Outline each uninfected red blood cell.
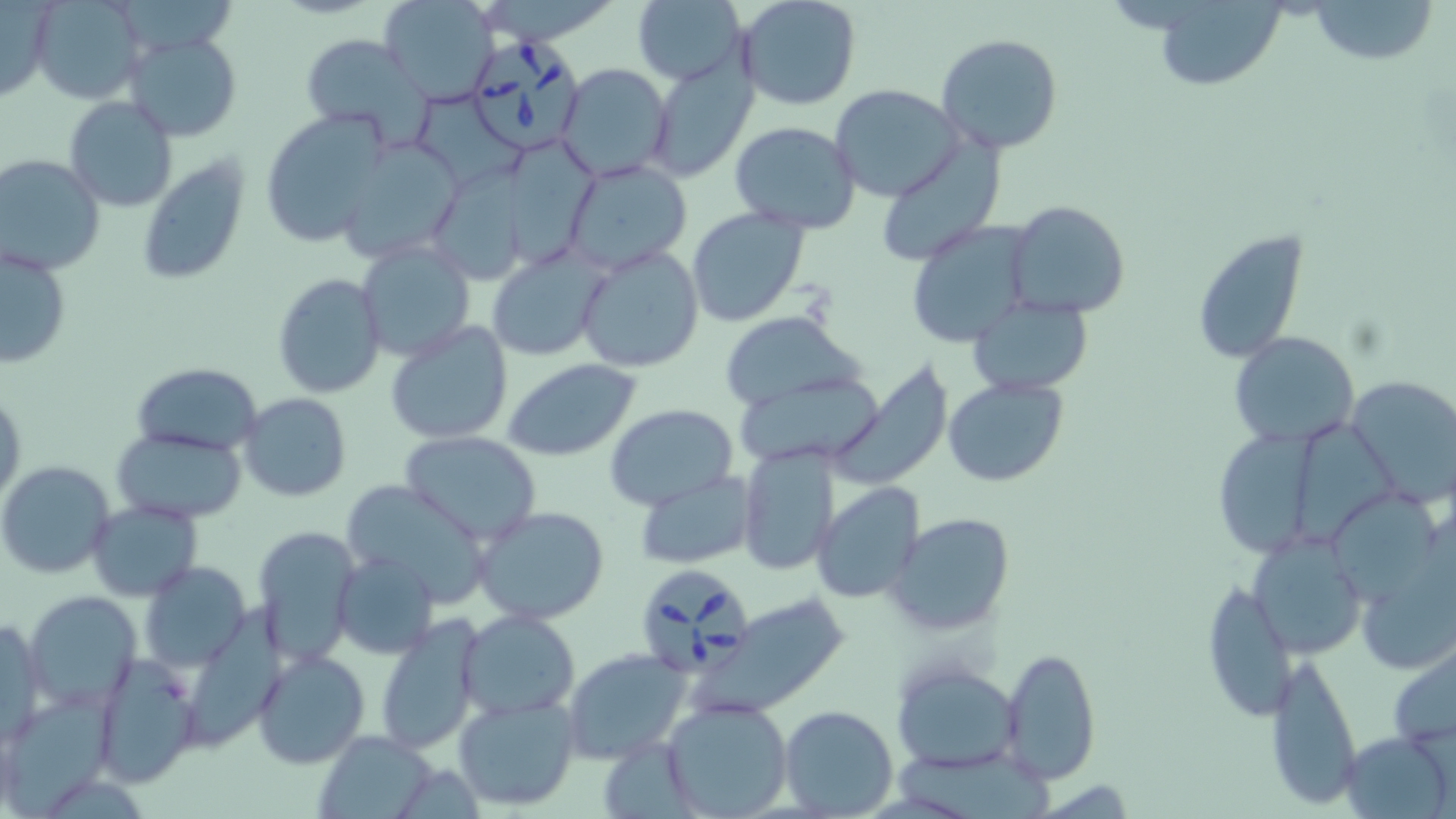

Approximate bounding boxes as (x1, y1, x2, y2) in pixels.
Uninfected red blood cells: (30, 0, 145, 104), (380, 0, 501, 107), (632, 0, 747, 86), (735, 0, 861, 112), (1305, 0, 1437, 67), (1152, 1, 1286, 90), (0, 3, 58, 105), (123, 32, 241, 143), (936, 33, 1065, 157), (298, 34, 439, 152), (647, 63, 757, 182), (556, 64, 673, 183), (830, 85, 964, 202), (63, 96, 178, 211), (420, 96, 527, 184), (258, 109, 393, 248), (729, 121, 860, 234), (333, 136, 463, 262), (510, 141, 598, 263), (873, 144, 1003, 265), (0, 154, 105, 276), (137, 154, 251, 285), (563, 160, 693, 275), (428, 169, 531, 287), (1005, 201, 1130, 317), (686, 206, 811, 326), (905, 219, 1034, 348), (1191, 229, 1309, 363), (355, 239, 476, 362), (1, 244, 72, 371), (576, 244, 705, 373), (485, 245, 609, 361), (270, 272, 388, 399), (968, 295, 1093, 397), (719, 310, 864, 412), (385, 318, 514, 445), (1229, 331, 1358, 449), (502, 358, 642, 460), (130, 362, 263, 455), (827, 364, 954, 490), (737, 372, 887, 471), (1345, 375, 1456, 509), (943, 376, 1069, 488), (1, 387, 25, 509), (240, 393, 351, 502), (606, 404, 738, 511), (1296, 426, 1404, 550), (1210, 428, 1319, 558), (111, 429, 249, 523), (399, 431, 543, 547), (737, 444, 840, 576), (0, 460, 116, 580), (634, 473, 759, 568), (342, 482, 495, 601), (810, 483, 925, 604), (1345, 496, 1445, 606), (87, 499, 202, 602), (474, 506, 610, 624), (887, 512, 1016, 636), (253, 526, 360, 665), (1249, 535, 1366, 660), (1356, 535, 1455, 673), (333, 550, 439, 659), (142, 560, 250, 670), (1201, 575, 1296, 725), (23, 589, 142, 713), (707, 594, 854, 715), (186, 598, 294, 755), (458, 610, 581, 719), (373, 614, 487, 756), (1, 618, 46, 743), (1387, 641, 1456, 751), (999, 646, 1101, 784), (251, 648, 372, 769), (562, 648, 692, 763), (1265, 650, 1363, 810), (90, 653, 203, 787), (891, 659, 1023, 771), (3, 692, 117, 811), (453, 693, 581, 808), (660, 699, 792, 818), (779, 705, 898, 818), (1339, 729, 1453, 818), (313, 731, 441, 819), (599, 736, 697, 819), (897, 750, 1059, 819).

Babesia divergens-infected red blood cell locations: (472, 31, 586, 153), (642, 567, 754, 686). Slide-level diagnosis: Babesia divergens. May-Grünwald-Giemsa stain. Image is 1456×819 pixels. Light microscopy. Captured at 1000x magnification. One field of a larger specimen. Thin blood film.